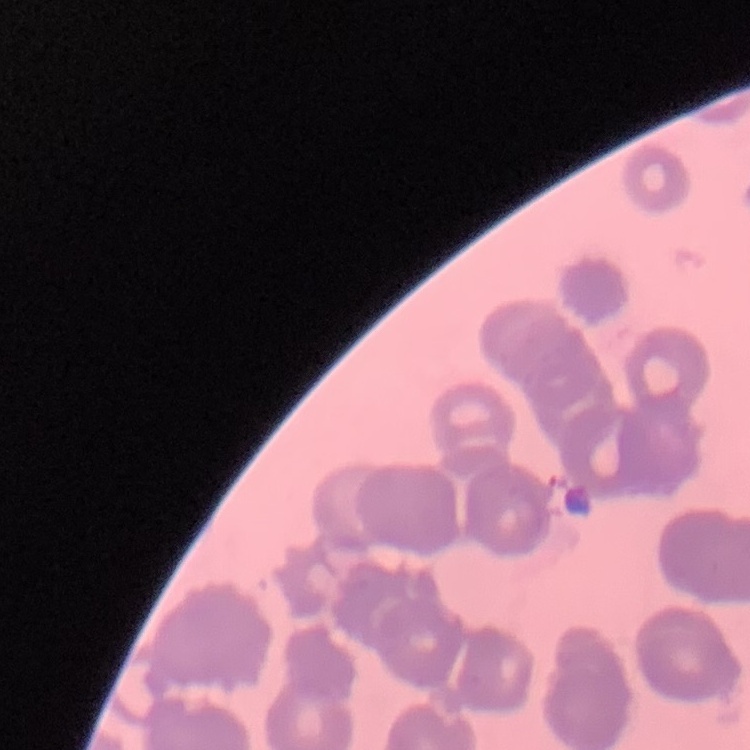 The erythrocytes exhibit rouleaux formation. Field's or Giemsa stain. One tile cut from a larger photomicrograph. Thin blood smear.